Classify this cell by malaria status.
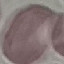
Uninfected.

stain: Giemsa
capture: smartphone camera at the microscope eyepiece
image_type: automatically extracted cell patch, resized to 64 × 64 pixels
preparation: thin smear